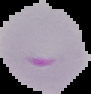

{
  "image_type": "segmented cell region on a black background",
  "malaria_status": "parasitized",
  "preparation": "thin blood film",
  "image_size": "91×94 pixels"
}